Classify this cell by malaria status.
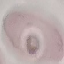
It is uninfected.

stain = Giemsa
capture = smartphone through the microscope eyepiece
image type = automatically extracted cell patch, resized to 64 × 64 pixels
preparation = thin blood smear